Assess the morphology of the red blood cells.
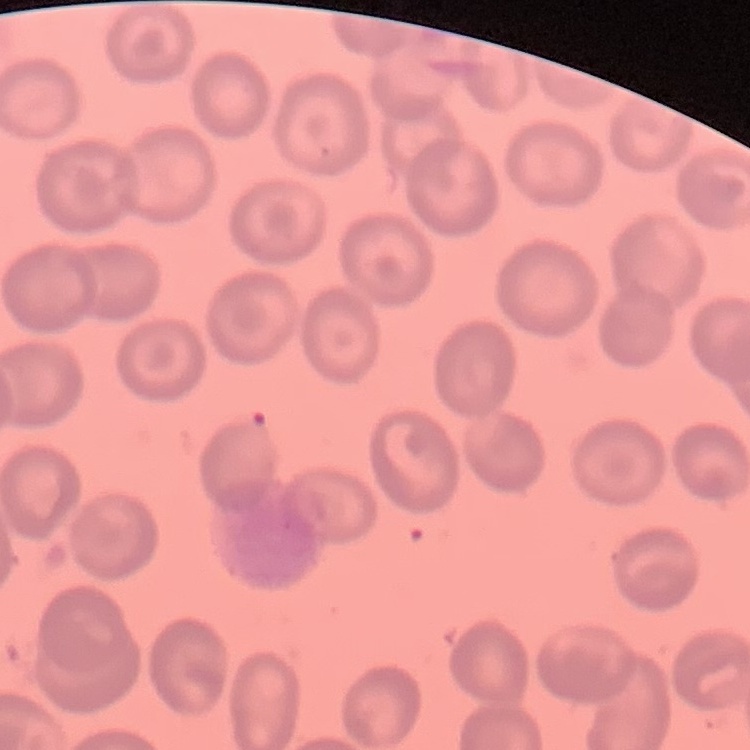

They show no rouleaux formation.

{
  "preparation": "thin peripheral smear",
  "image_type": "one tile cut from a larger photomicrograph",
  "stain": "Field's or Giemsa"
}